Give the position of every malaria parasite.
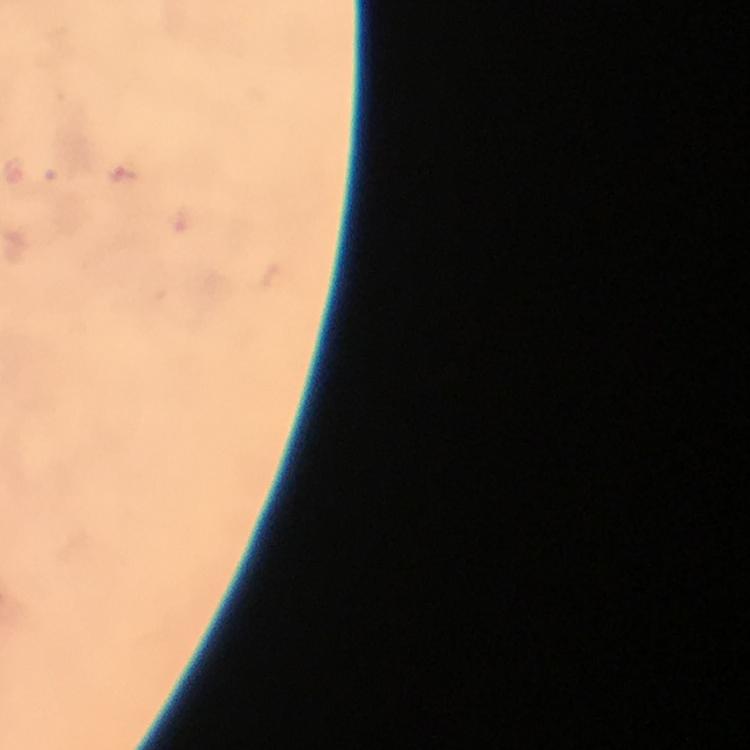

Approximate object centers, in pixels from the top-left corner.
Malaria parasites: (x=125, y=177).

image_size: 750×750 pixels
context: from a malaria diagnostic workup
stain: Giemsa
preparation: thick blood smear
immersion_oil: applied
cropped_from: a single field of view
capture: smartphone camera through the microscope
magnification: 100x